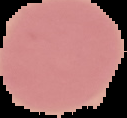
From a thin blood film. Malaria status: uninfected. The area outside the segmented cell region is set to black. Image is 127×118 pixels.